State which cell type is depicted.
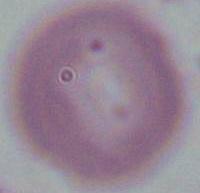
An erythrocyte.

modality: micrograph
magnification: 1000x